Report the malaria status of this cell.
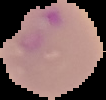

Parasitized.

From a thin blood smear. Cell region segmented out of the field of view; the surrounding area is masked to black. Image is 106×100 pixels.